Report the malaria status of this cell.
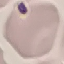
It is uninfected.

Thin blood film. Acquired by smartphone through the microscope eyepiece. Giemsa-stained preparation. Automatically extracted cell patch, resized to 64 × 64 pixels.